Comment on the morphology of the erythrocytes.
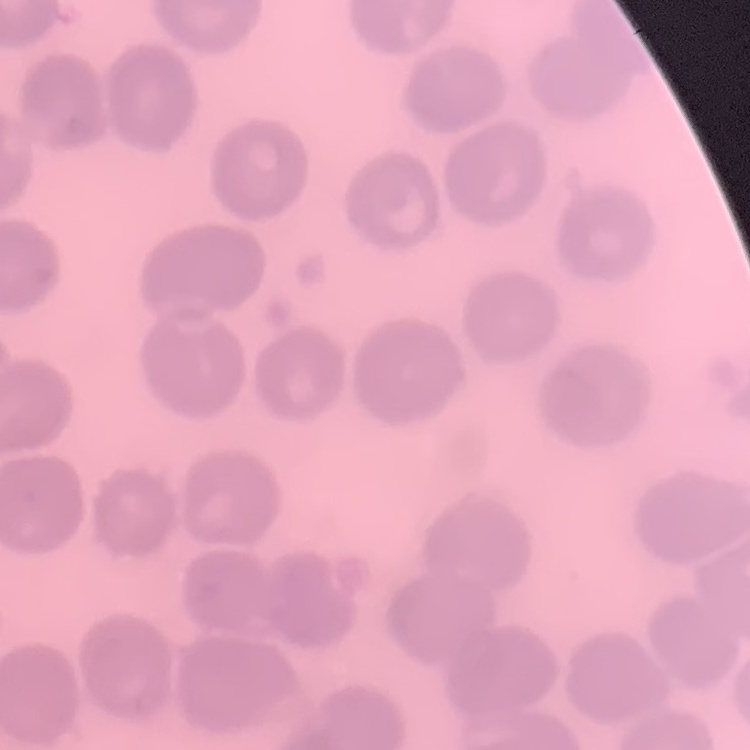
They show no rouleaux formation.

Thin blood smear. One tile cut from a larger photomicrograph. Field's or Giemsa stain.